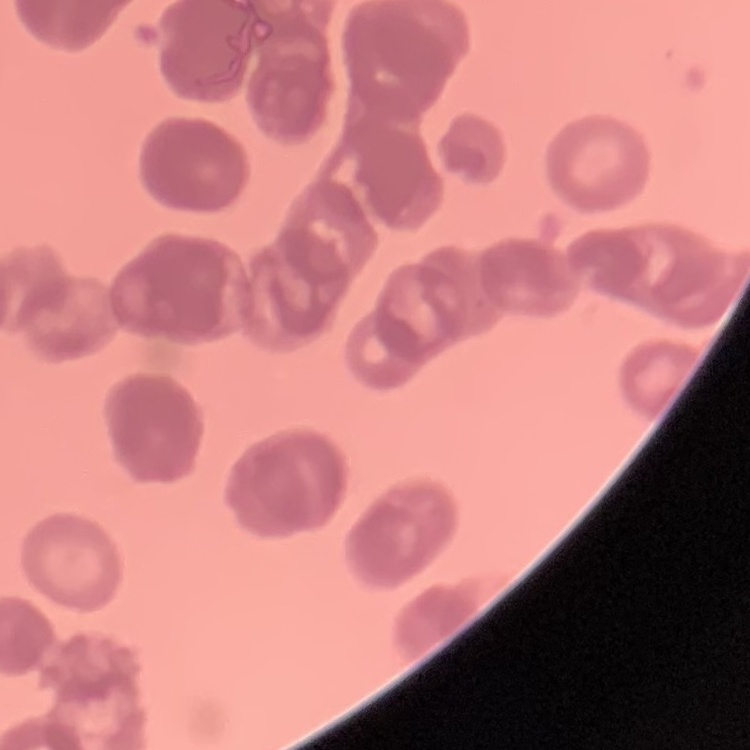
Summary:
  - Erythrocyte morphology: rouleaux formation
  - Preparation: thin blood smear
  - Stain: Field's or Giemsa
  - Image type: one tile cut from a larger photomicrograph